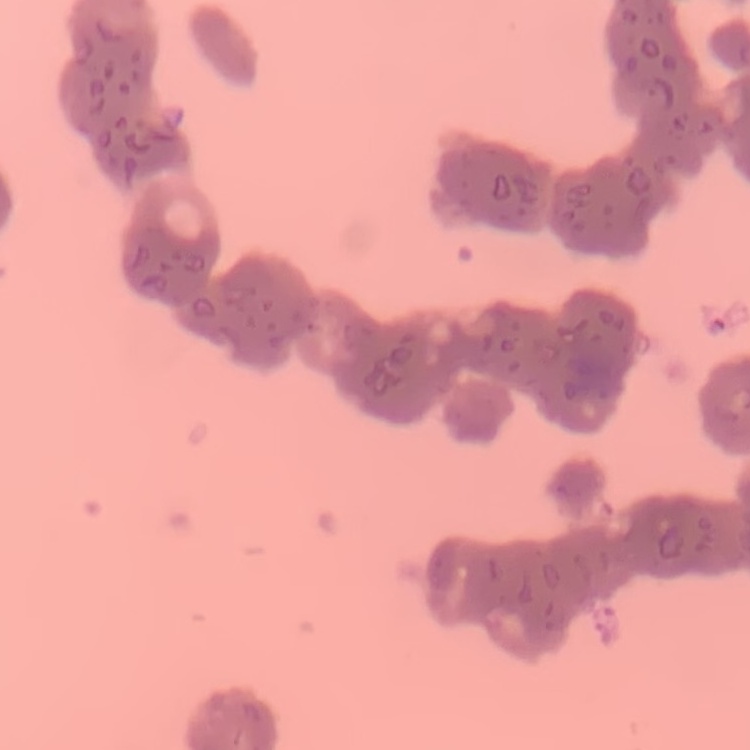
erythrocyte morphology = rouleaux formation
stain = Field's or Giemsa
image type = one tile cut from a larger photomicrograph
preparation = thin peripheral smear